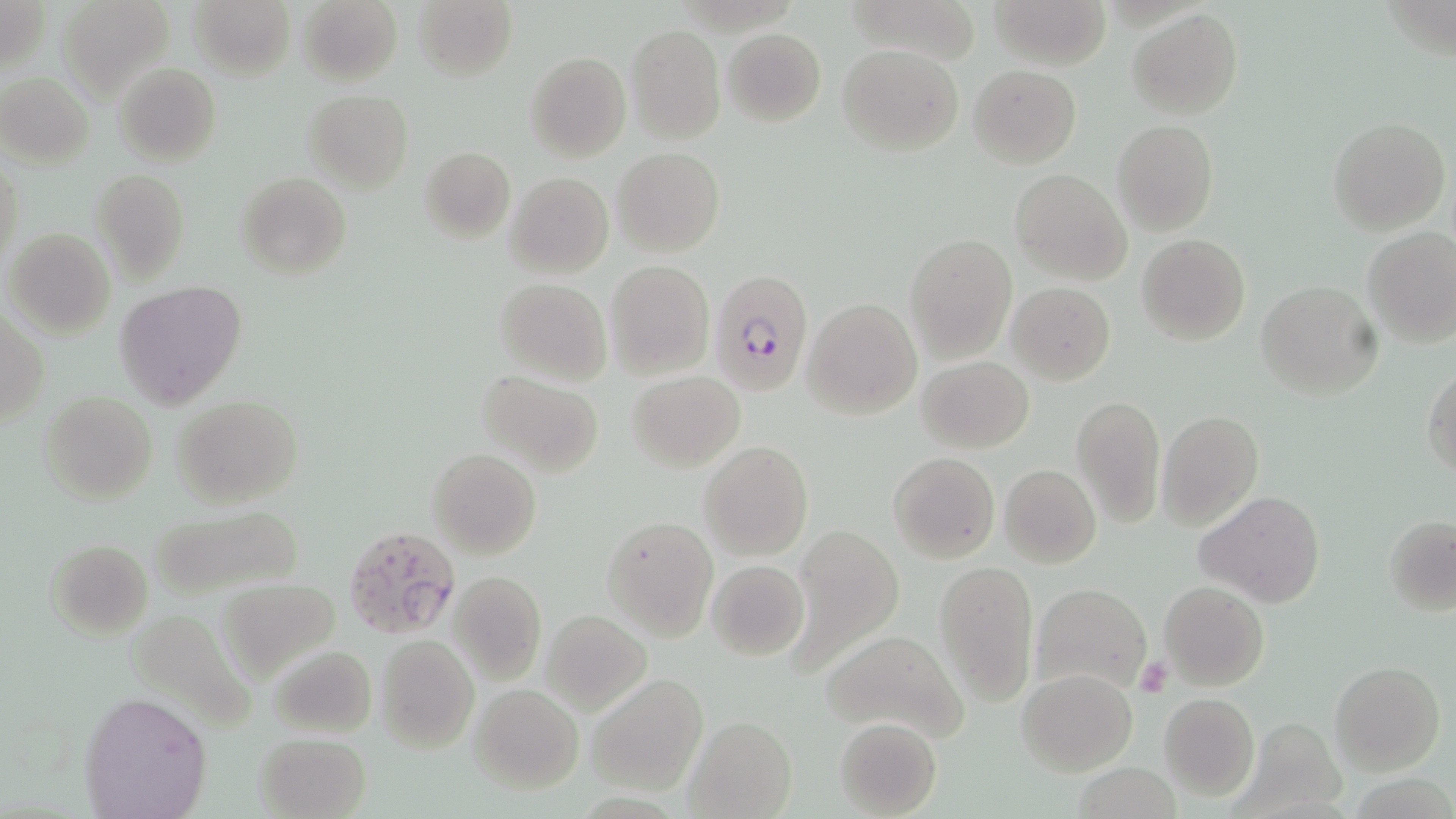

Summary:
  - Coordinate format: approximate bounding boxes as named x1/y1/x2/y2 corners in pixels
  - Plasmodium falciparum-infected red blood cell locations: (x1=708, y1=267, x2=813, y2=396), (x1=343, y1=524, x2=461, y2=641)
  - Platelet locations: (x1=1134, y1=656, x2=1171, y2=697)
  - Uninfected red blood cell locations: (x1=2, y1=0, x2=48, y2=75), (x1=58, y1=0, x2=174, y2=102), (x1=190, y1=0, x2=294, y2=79), (x1=297, y1=0, x2=402, y2=87), (x1=992, y1=0, x2=1109, y2=69), (x1=412, y1=1, x2=517, y2=82), (x1=1127, y1=9, x2=1243, y2=120), (x1=626, y1=24, x2=725, y2=143), (x1=723, y1=29, x2=826, y2=126), (x1=835, y1=44, x2=963, y2=156), (x1=524, y1=51, x2=631, y2=163), (x1=115, y1=63, x2=221, y2=166), (x1=969, y1=65, x2=1080, y2=168), (x1=0, y1=73, x2=94, y2=166), (x1=303, y1=90, x2=413, y2=194), (x1=1329, y1=117, x2=1450, y2=235), (x1=1111, y1=119, x2=1218, y2=236), (x1=419, y1=146, x2=515, y2=243), (x1=613, y1=147, x2=724, y2=257), (x1=1, y1=157, x2=22, y2=270), (x1=508, y1=160, x2=725, y2=264), (x1=90, y1=168, x2=189, y2=285), (x1=1010, y1=169, x2=1130, y2=284), (x1=505, y1=172, x2=613, y2=278), (x1=237, y1=174, x2=350, y2=279), (x1=1362, y1=226, x2=1456, y2=347), (x1=6, y1=229, x2=115, y2=339), (x1=905, y1=234, x2=1016, y2=362), (x1=1137, y1=234, x2=1250, y2=345), (x1=605, y1=260, x2=714, y2=379), (x1=495, y1=277, x2=611, y2=385), (x1=116, y1=280, x2=245, y2=410), (x1=1255, y1=282, x2=1382, y2=399), (x1=1008, y1=283, x2=1115, y2=384), (x1=805, y1=298, x2=922, y2=419), (x1=1, y1=310, x2=48, y2=428), (x1=916, y1=356, x2=1034, y2=453), (x1=1423, y1=365, x2=1456, y2=478), (x1=474, y1=370, x2=605, y2=477), (x1=627, y1=370, x2=744, y2=470), (x1=43, y1=393, x2=157, y2=505), (x1=1071, y1=393, x2=1167, y2=528), (x1=173, y1=395, x2=304, y2=509), (x1=1157, y1=410, x2=1263, y2=530), (x1=700, y1=441, x2=813, y2=562), (x1=428, y1=449, x2=540, y2=560), (x1=888, y1=452, x2=999, y2=564), (x1=999, y1=464, x2=1101, y2=569), (x1=1197, y1=492, x2=1326, y2=608), (x1=146, y1=506, x2=307, y2=600), (x1=603, y1=516, x2=719, y2=639), (x1=1384, y1=516, x2=1455, y2=614), (x1=788, y1=527, x2=904, y2=673), (x1=47, y1=539, x2=152, y2=640), (x1=706, y1=560, x2=810, y2=661), (x1=934, y1=560, x2=1038, y2=707), (x1=449, y1=571, x2=547, y2=686), (x1=220, y1=580, x2=341, y2=680), (x1=1030, y1=580, x2=1152, y2=695), (x1=1158, y1=581, x2=1269, y2=691), (x1=543, y1=610, x2=652, y2=715), (x1=821, y1=628, x2=969, y2=743), (x1=376, y1=635, x2=478, y2=752), (x1=267, y1=644, x2=377, y2=738), (x1=1331, y1=661, x2=1443, y2=775), (x1=1017, y1=668, x2=1138, y2=775), (x1=588, y1=675, x2=708, y2=793), (x1=469, y1=684, x2=583, y2=792), (x1=79, y1=689, x2=212, y2=818), (x1=1159, y1=694, x2=1258, y2=799), (x1=683, y1=715, x2=797, y2=818), (x1=834, y1=718, x2=941, y2=817), (x1=254, y1=731, x2=370, y2=818)
  - Slide-level diagnosis: Plasmodium falciparum
  - Field of view: one of a larger specimen
  - Magnification: 1000x
  - Modality: optical microscopy
  - Preparation: thin blood film
  - Stain: May-Grünwald-Giemsa
  - Image size: 1456×819 pixels